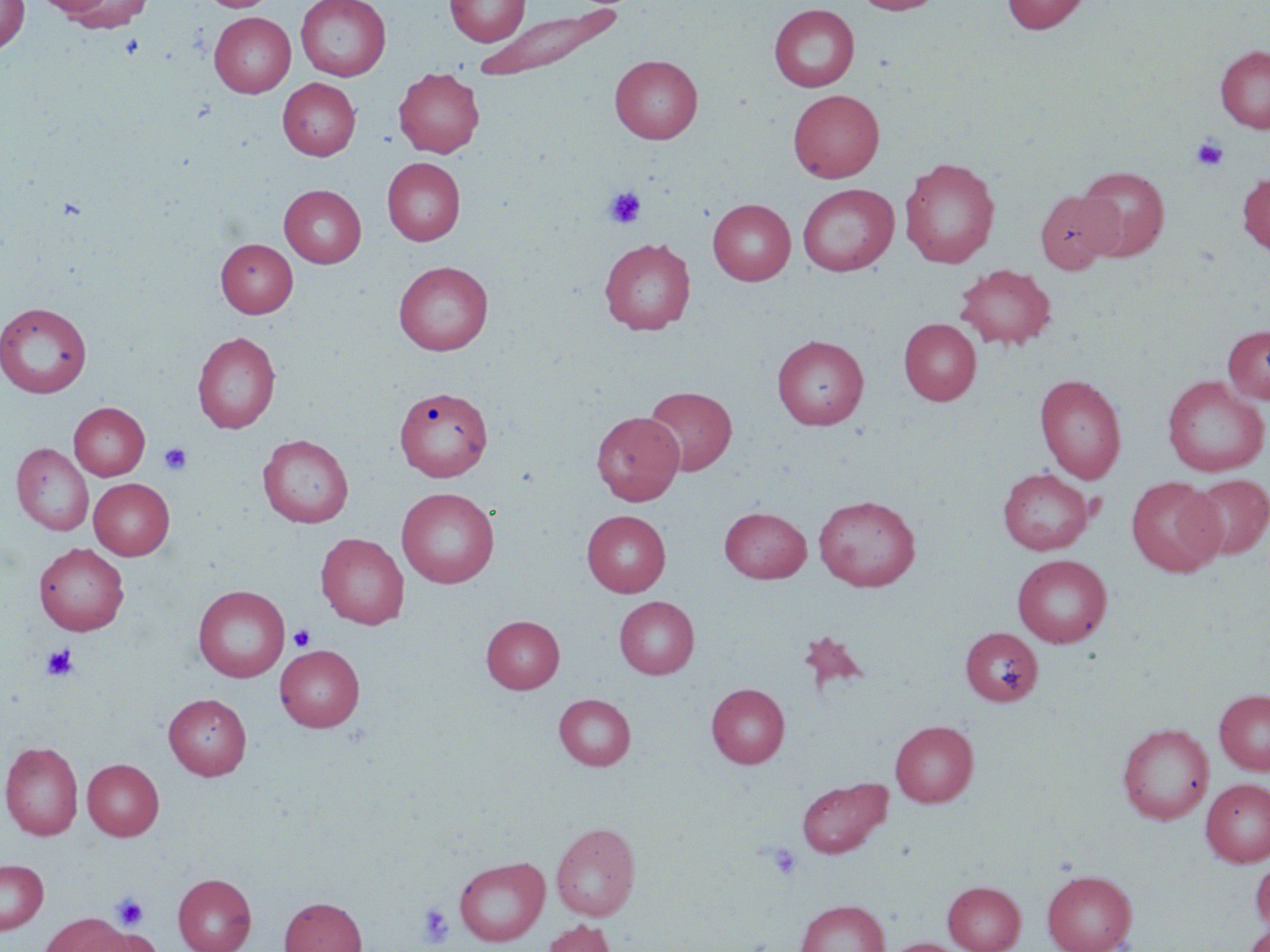
Approximate bounding boxes as (x1, y1, x2, y2) in pixels. Platelet locations: (1191, 135, 1229, 171), (603, 185, 646, 229), (159, 443, 192, 475), (289, 624, 315, 651), (41, 644, 78, 681), (766, 843, 802, 881), (111, 894, 148, 931), (418, 903, 455, 948). Uninfected red blood cell locations: (0, 0, 30, 54), (34, 0, 114, 16), (62, 0, 153, 32), (201, 0, 277, 12), (296, 0, 391, 81), (444, 0, 530, 46), (853, 0, 943, 15), (1002, 0, 1089, 34), (475, 4, 622, 82), (769, 4, 860, 92), (209, 12, 295, 97), (1215, 45, 1270, 132), (609, 55, 703, 143), (393, 67, 484, 157), (389, 68, 473, 244), (278, 78, 360, 160), (788, 89, 885, 182), (899, 156, 1000, 268), (382, 157, 465, 246), (1077, 165, 1171, 261), (1237, 172, 1270, 257), (797, 183, 899, 276), (279, 185, 366, 268), (1035, 190, 1121, 273), (707, 198, 796, 285), (216, 238, 297, 317), (598, 238, 696, 335), (393, 261, 493, 355), (956, 263, 1056, 350), (0, 302, 91, 398), (899, 318, 981, 405), (1222, 325, 1270, 404), (192, 331, 281, 433), (772, 334, 869, 430), (1035, 373, 1126, 483), (1162, 376, 1268, 477), (395, 385, 492, 481), (643, 386, 737, 475), (68, 402, 150, 480), (591, 411, 684, 504), (258, 434, 353, 528), (11, 443, 94, 536), (997, 469, 1094, 555), (1184, 475, 1270, 560), (1125, 477, 1225, 577), (89, 478, 175, 560), (396, 487, 500, 588), (813, 494, 921, 591), (719, 507, 811, 582), (581, 510, 670, 596), (315, 532, 409, 629), (34, 543, 129, 635), (1012, 554, 1112, 647), (193, 585, 290, 682), (614, 596, 699, 679), (481, 615, 564, 693), (960, 627, 1043, 706), (797, 630, 869, 698), (275, 644, 365, 731), (706, 683, 790, 768), (1214, 689, 1270, 775), (164, 693, 251, 779), (554, 693, 636, 770), (890, 720, 978, 807), (1117, 723, 1214, 824), (0, 740, 83, 840), (83, 759, 164, 840), (797, 776, 891, 858), (1201, 778, 1270, 867), (551, 822, 641, 921), (454, 856, 549, 946), (0, 859, 48, 934), (1250, 860, 1270, 937), (1042, 869, 1138, 952), (173, 873, 256, 952), (943, 881, 1025, 952), (279, 897, 366, 952), (795, 899, 889, 952), (39, 913, 136, 952), (541, 919, 617, 952), (1243, 920, 1270, 952), (90, 927, 162, 952), (883, 938, 968, 952). Slide-level diagnosis: no evidence of blood parasites. May-Grünwald-Giemsa stain. Thin blood film. Optical microscopy. Single field of view. 1000x magnification. Image is 1270×952 pixels.